Report the malaria status of this cell.
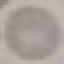
It is uninfected.

{
  "preparation": "thin blood smear",
  "stain": "Giemsa",
  "image_type": "automatically extracted cell patch, resized to 64 × 64 pixels",
  "capture": "smartphone through the microscope eyepiece"
}